Give the position of every Plasmodium parasite and every leukocyte.
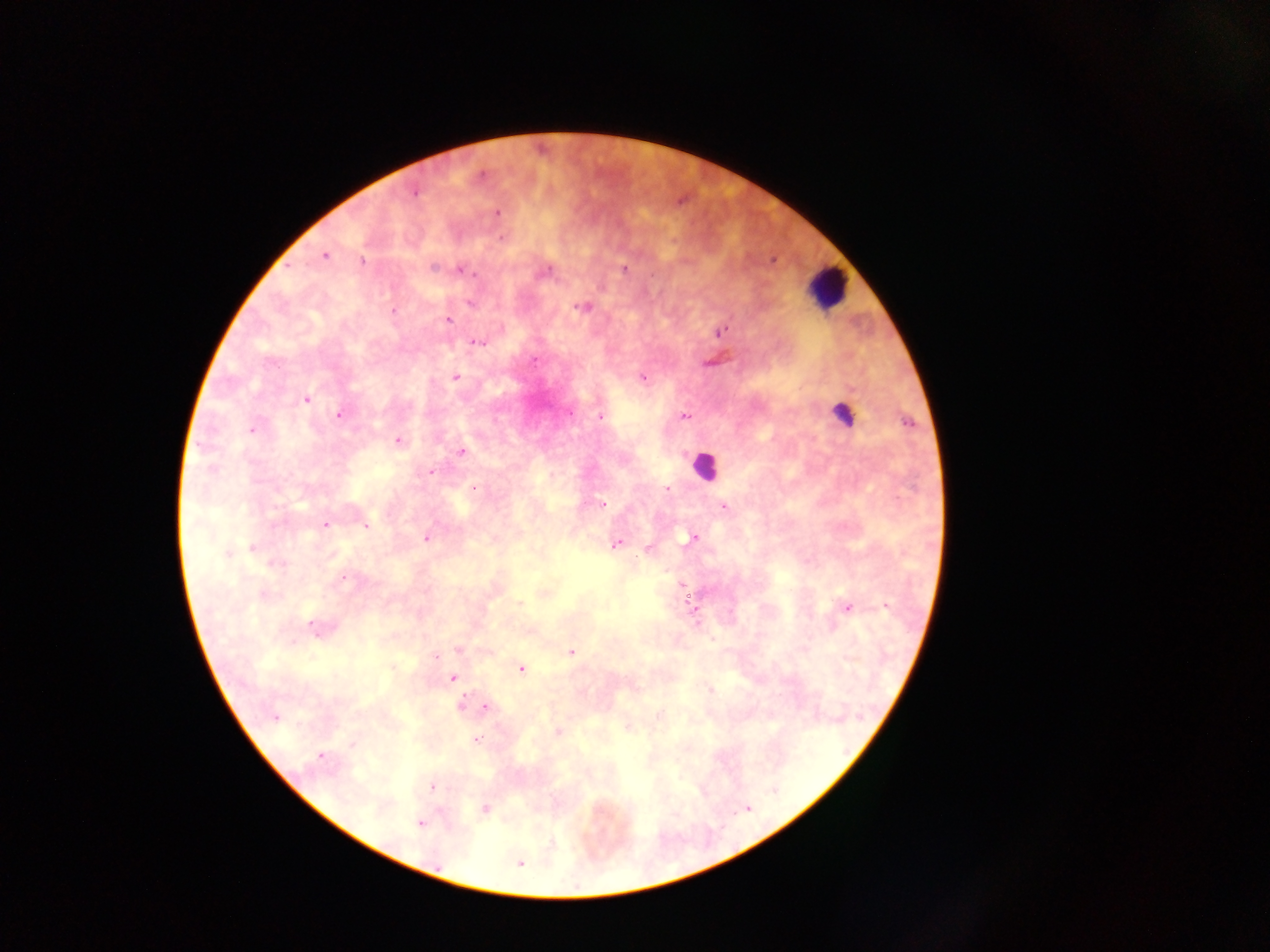

Approximate centers as {x, y} in pixels.
Plasmodium parasites: {481, 175}, {414, 192}, {496, 213}, {503, 238}, {324, 255}, {362, 261}, {433, 268}, {625, 269}, {462, 271}, {471, 302}, {583, 307}, {394, 310}, {447, 320}, {720, 330}, {478, 342}, {534, 359}, {456, 377}, {642, 378}, {306, 399}, {570, 413}, {340, 415}, {601, 417}, {685, 417}, {908, 422}, {251, 430}, {397, 441}, {461, 451}, {430, 473}, {474, 488}, {668, 489}, {602, 504}, {724, 507}, {325, 524}, {366, 526}, {426, 538}, {693, 538}, {616, 545}, {253, 548}, {648, 548}, {227, 554}, {276, 564}, {343, 577}, {682, 584}, {264, 595}, {519, 603}, {692, 605}, {886, 606}, {847, 607}, {312, 628}, {458, 650}, {572, 652}, {435, 656}, {521, 669}, {453, 677}, {709, 689}, {463, 703}, {486, 706}, {660, 715}, {274, 718}, {558, 732}, {477, 740}, {353, 745}, {320, 756}, {431, 786}, {485, 809}, {420, 824}, {520, 863}.
Leukocytes: {827, 288}, {841, 409}, {706, 466}.

Summary:
  - Field of view: single
  - Preparation: thick blood film
  - Country: Ghana
  - Image size: 1270×952 pixels
  - Capture: mobile-phone photograph through a microscope